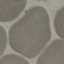
Summary:
  - Malaria status: uninfected
  - Capture: smartphone camera at the microscope eyepiece
  - Preparation: thin smear
  - Stain: Giemsa
  - Image type: cell patch, automatically extracted from a larger field of view and resized to 64 × 64 pixels